Classify this cell by malaria status.
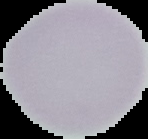

Uninfected.

Summary:
  - Image type: cell region segmented out of the field of view; surrounding area masked to black
  - Preparation: thin blood film
  - Image size: 148×139 pixels